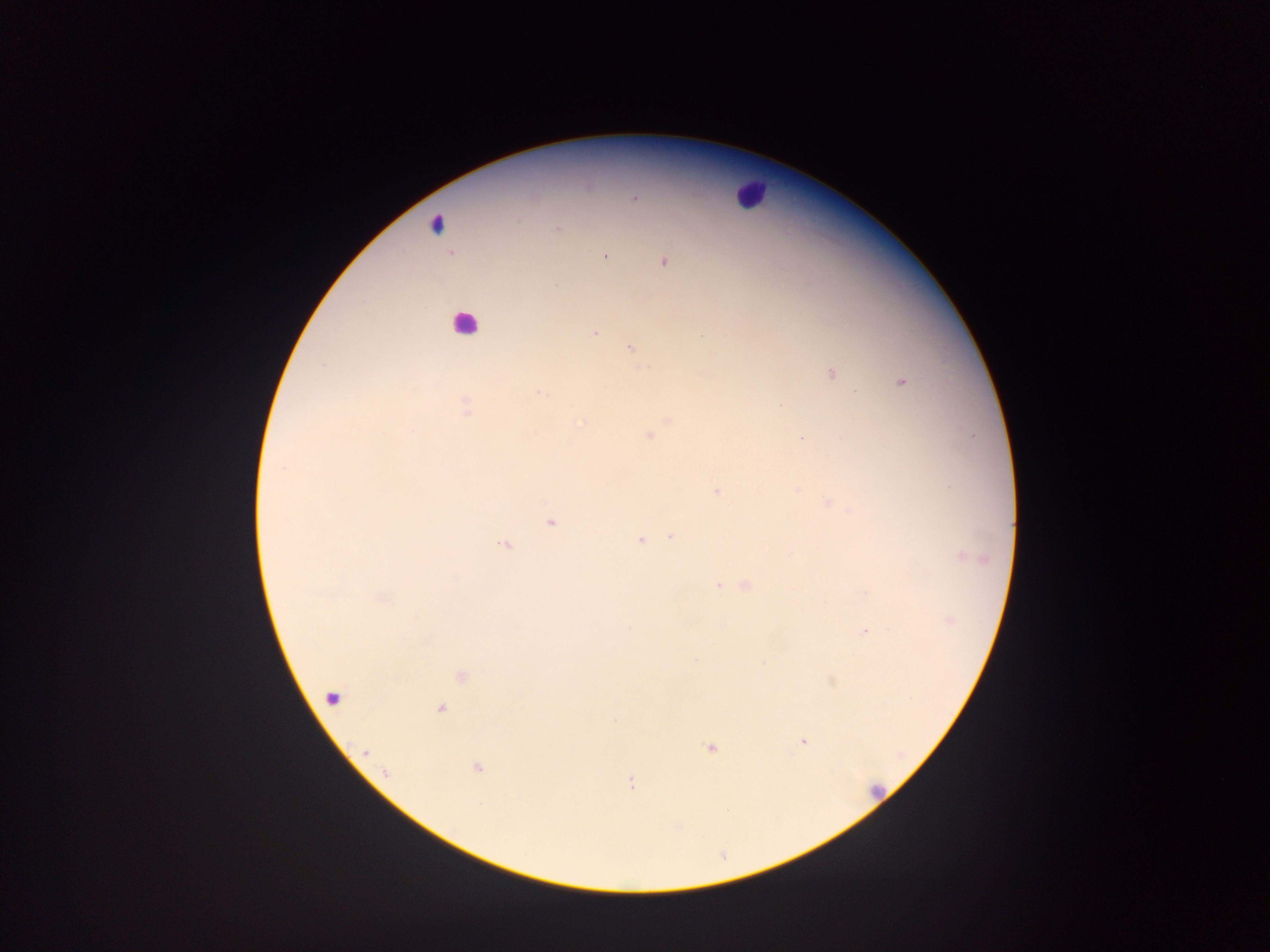

Approximate centers as [x, y] in pixels. Malaria parasite locations: [634, 197], [557, 229], [605, 255], [664, 262], [556, 284], [594, 333], [631, 349], [326, 365], [831, 373], [902, 381], [539, 393], [780, 405], [465, 408], [668, 420], [582, 424], [650, 436], [803, 438], [716, 492], [830, 504], [551, 522], [671, 537], [640, 540], [504, 544], [963, 556], [747, 585], [718, 586], [866, 632], [461, 676], [440, 709], [615, 721], [804, 741], [711, 747], [477, 768], [630, 782]. Leukocyte locations: [749, 194], [437, 223], [467, 321], [334, 697], [875, 792]. Thick blood film. Mobile-phone photograph taken through the microscope. Single field of view. Image is 1270×952 pixels. Sample from Ghana.